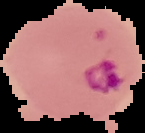

Summary:
  - Preparation: thin blood smear
  - Image type: segmented cell region with the area outside set to black
  - Result: Plasmodium parasites detected
  - Image size: 145×133 pixels